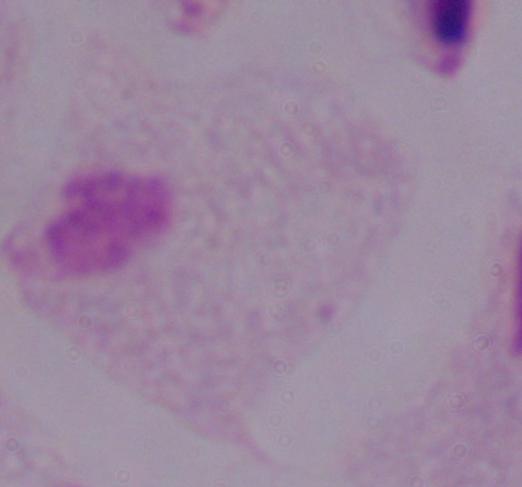

magnification = 1000x
modality = micrograph
identification = trichomonad